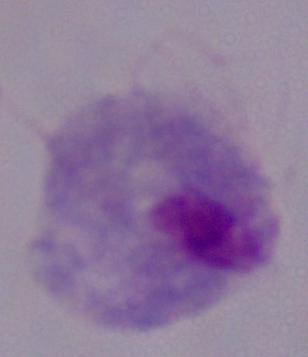 1000x magnification. A trichomonad is shown. Photomicrograph.